Describe the morphology of the erythrocytes.
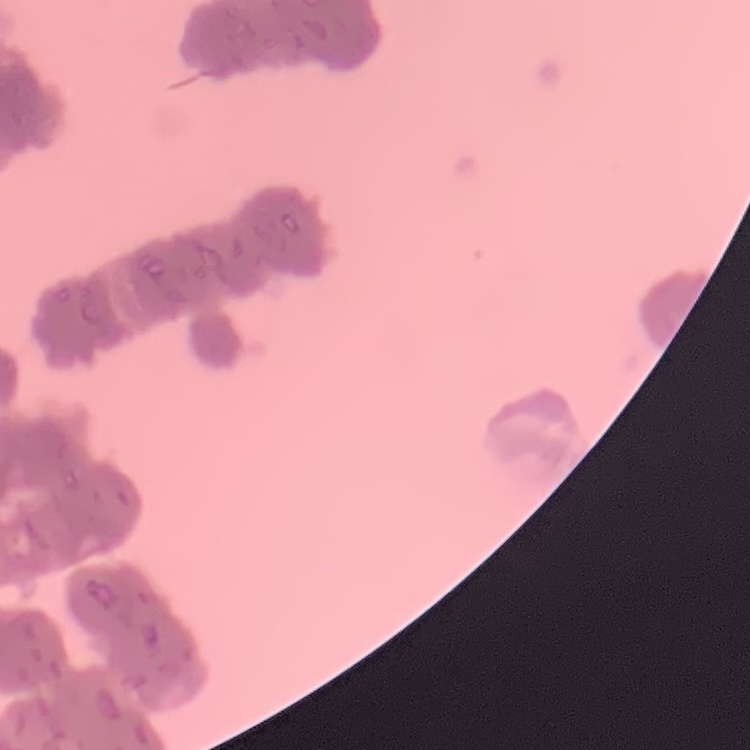

They show rouleaux formation.

Thin blood film. One tile cut from a larger photomicrograph. Field's or Giemsa stain.